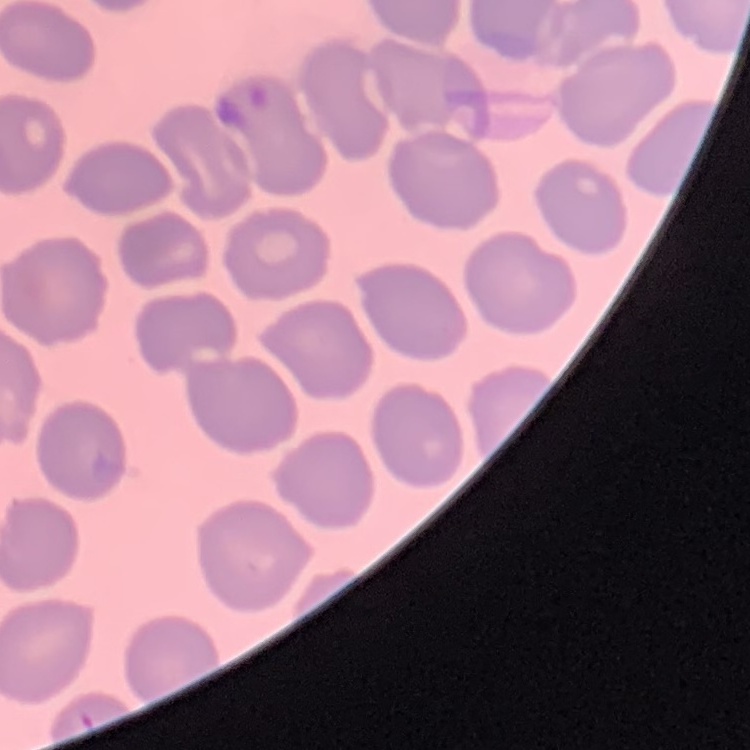

The erythrocytes show no rouleaux formation. Stained with either Field's or Giemsa. Thin blood smear. One tile cut from a larger photomicrograph.